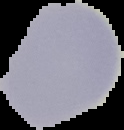
Summary:
  - Image type: segmented cell region on a black background
  - Preparation: thin blood film
  - Image size: 124×130 pixels
  - Malaria status: uninfected